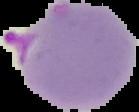

Summary:
  - Image type: segmented cell region on a black background
  - Result: Plasmodium parasites identified
  - Preparation: thin blood smear
  - Image size: 139×112 pixels